Outline each Plasmodium falciparum-infected red blood cell.
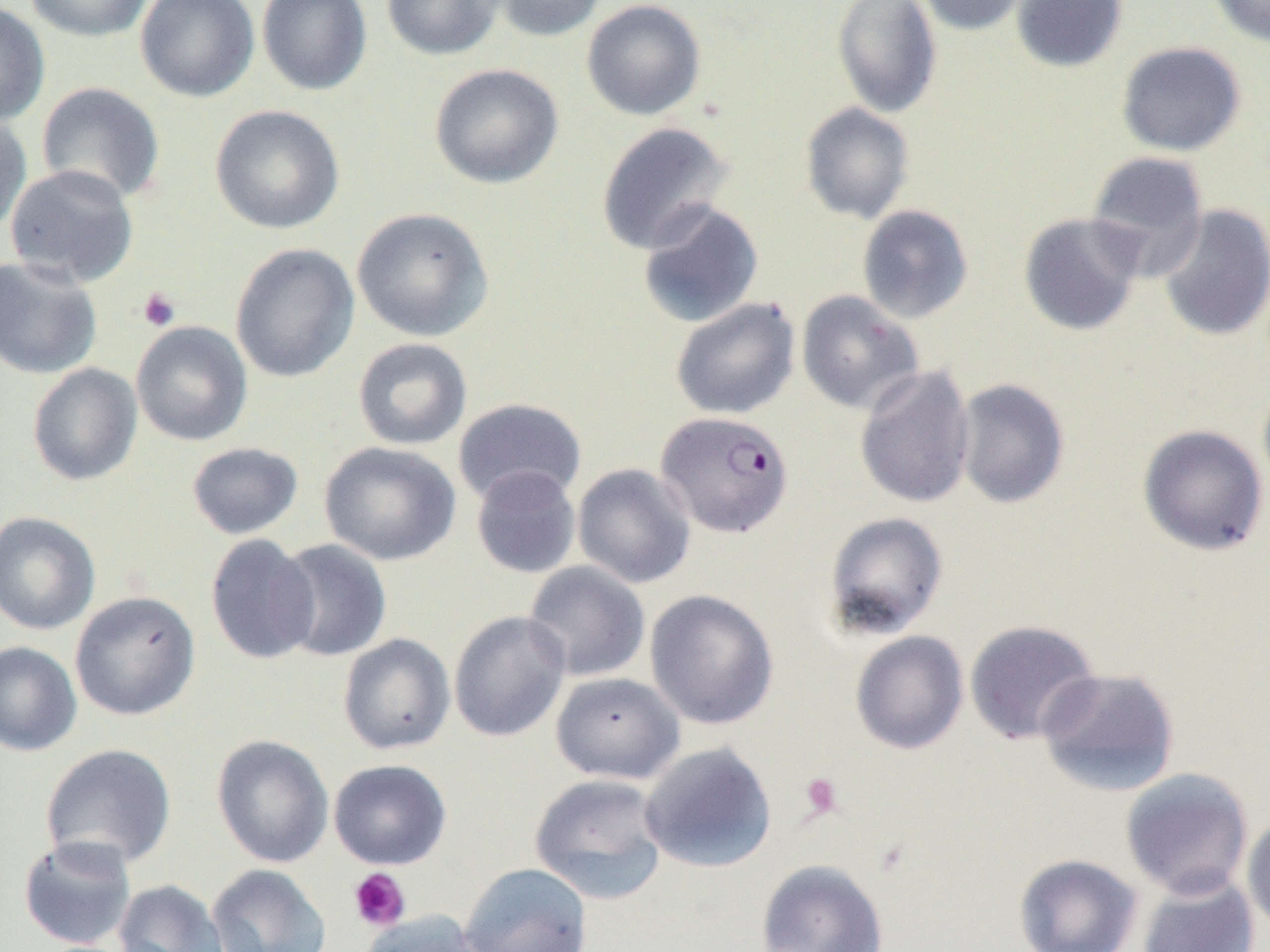

Approximate bounding boxes as (x1,y1)-(x2,y2) corner pairs in pixels.
Plasmodium falciparum-infected red blood cells: (655,410)-(793,537).

slide-level diagnosis = Plasmodium falciparum
preparation = thin blood film
field of view = one of a larger specimen
image size = 1270×952 pixels
platelet locations = approximate bounding boxes as (x1,y1)-(x2,y2) corner pairs in pixels: (137,287)-(181,332), (799,772)-(844,820), (348,867)-(410,931)
modality = light microscopy
magnification = 1000x
uninfected red blood cell locations = approximate bounding boxes as (x1,y1)-(x2,y2) corner pairs in pixels: (24,0)-(153,42), (135,0)-(260,102), (257,0)-(372,95), (381,0)-(504,61), (490,0)-(608,42), (581,0)-(706,120), (831,0)-(942,118), (915,0)-(1033,35), (1011,0)-(1128,73), (1207,0)-(1270,46), (0,2)-(50,127), (1116,41)-(1246,156), (429,63)-(563,189), (36,82)-(166,206), (800,102)-(915,224), (209,104)-(345,234), (0,111)-(32,237), (595,121)-(734,255), (1085,150)-(1209,277), (4,164)-(140,287), (636,200)-(764,329), (1157,204)-(1270,342), (856,205)-(974,324), (351,207)-(494,342), (1018,212)-(1146,337), (230,242)-(360,383), (0,256)-(103,379), (796,290)-(924,416), (670,297)-(800,420), (130,321)-(254,446), (352,337)-(473,451), (26,363)-(143,486), (854,365)-(975,509), (953,378)-(1070,509), (1257,379)-(1270,499), (452,398)-(587,506), (1137,424)-(1268,556), (319,441)-(461,566), (186,442)-(304,539), (572,463)-(696,588), (470,465)-(581,579), (0,511)-(101,635), (823,511)-(949,640), (205,534)-(321,665), (273,539)-(393,662), (522,561)-(650,682), (644,589)-(779,730), (70,590)-(200,721), (448,611)-(571,743), (964,620)-(1102,746), (850,630)-(969,755), (337,633)-(456,755), (0,641)-(82,757), (1036,667)-(1181,797), (551,671)-(684,784), (211,734)-(334,868), (639,741)-(778,873), (40,743)-(177,870), (328,759)-(452,870), (1120,767)-(1255,900), (528,772)-(670,904), (1241,812)-(1270,937), (17,835)-(137,950), (1013,853)-(1143,952), (755,859)-(889,952), (458,862)-(593,952), (206,863)-(332,952), (1136,871)-(1260,952), (113,879)-(229,952), (356,910)-(487,952)